State which parasite is depicted.
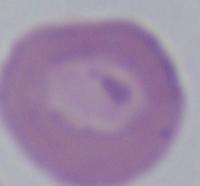

This is Babesia.

Micrograph. Captured at 1000x magnification.